Classify this cell by malaria status.
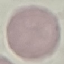

It is uninfected.

Giemsa stain. Acquired by smartphone through the microscope eyepiece. Thin blood film. Cell patch, automatically extracted from a larger field of view and resized to 64 × 64 pixels.